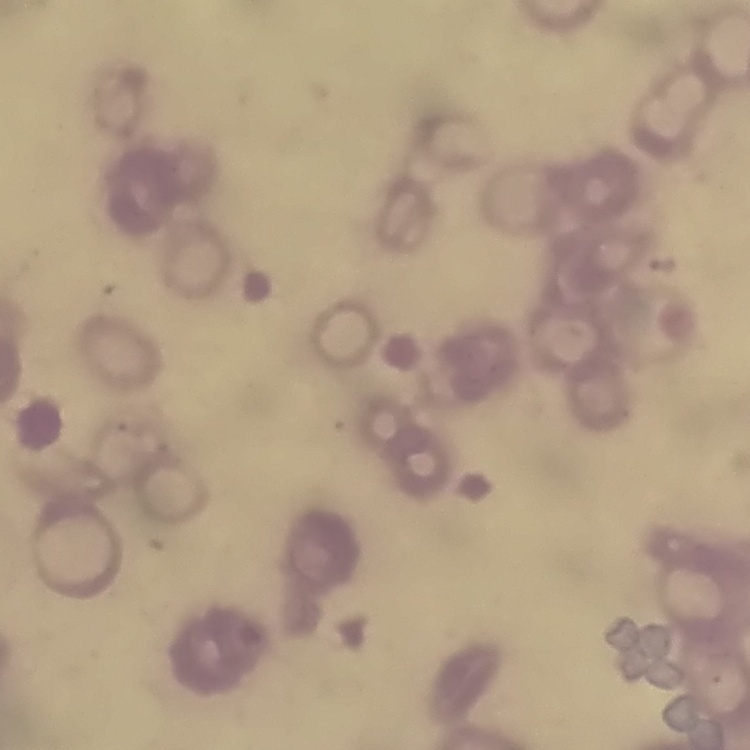

erythrocyte morphology = rouleaux formation
preparation = thin blood film
stain = Field's or Giemsa
image type = one tile cut from a larger photomicrograph